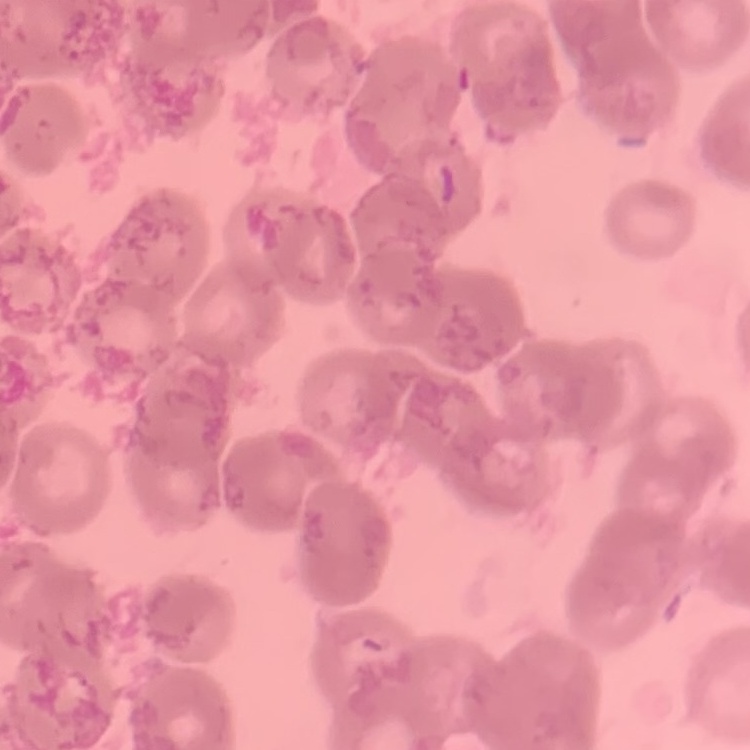
erythrocyte morphology = rouleaux formation
preparation = thin blood smear
stain = Field's or Giemsa
image type = one tile cut from a larger photomicrograph